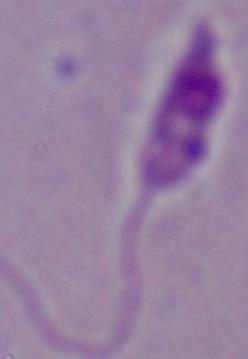
{
  "modality": "micrograph",
  "identification": "Leishmania",
  "magnification": "1000x"
}